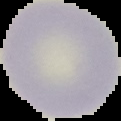
Summary:
  - Image size: 121×121 pixels
  - Malaria status: uninfected
  - Preparation: thin blood film
  - Image type: cell region segmented out of the field of view; surrounding area masked to black